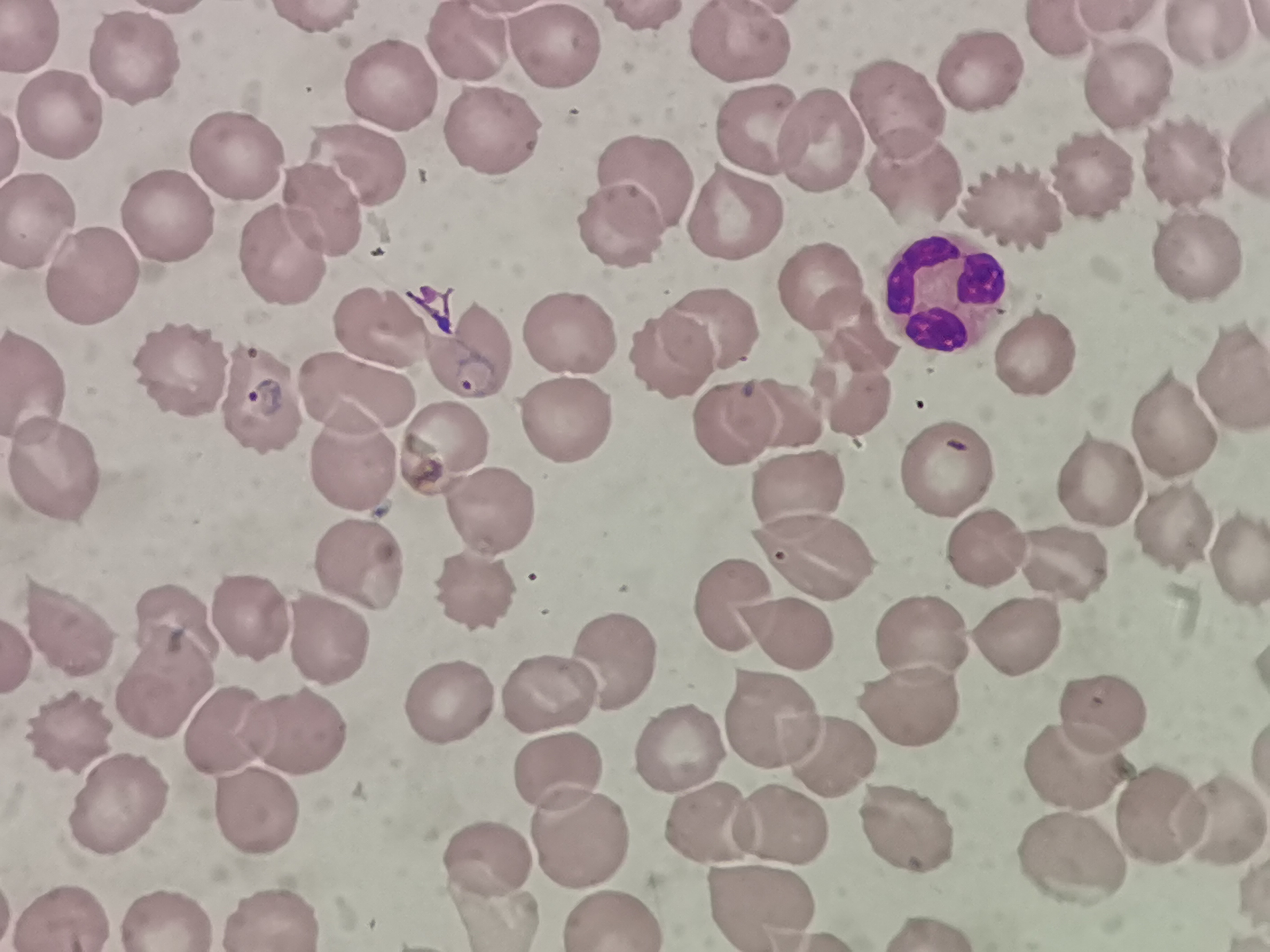
Approximate centers as {x, y} in pixels. Cell locations: {642, 18}, {321, 21}, {1058, 29}, {1203, 37}, {744, 44}, {467, 45}, {552, 47}, {136, 62}, {973, 72}, {1121, 85}, {391, 92}, {897, 109}, {63, 122}, {765, 134}, {817, 134}, {497, 138}, {236, 162}, {1180, 166}, {353, 171}, {1098, 175}, {911, 181}, {642, 186}, {1013, 197}, {324, 212}, {172, 216}, {738, 218}, {41, 223}, {618, 231}, {286, 257}, {1195, 258}, {86, 275}, {935, 287}, {823, 291}, {712, 324}, {855, 328}, {568, 329}, {387, 334}, {471, 350}, {1037, 352}, {671, 359}, {183, 372}, {1225, 378}, {36, 385}, {361, 390}, {852, 396}, {784, 412}, {562, 413}, {721, 426}, {1173, 431}, {437, 444}, {351, 456}, {946, 470}, {59, 474}, {798, 482}, {1092, 485}, {490, 511}, {1173, 525}, {812, 546}, {986, 554}, {1241, 557}, {1061, 562}, {356, 571}, {477, 593}, {731, 601}, {246, 621}, {70, 626}, {178, 630}, {786, 630}, {316, 637}, {1017, 638}, {921, 640}, {614, 654}, {158, 683}, {908, 695}, {550, 696}, {445, 700}, {1104, 707}, {768, 721}, {222, 729}, {295, 733}, {73, 736}, {675, 744}, {826, 753}, {1077, 760}, {556, 767}, {122, 799}, {251, 806}, {1157, 814}, {784, 817}, {1217, 817}, {911, 821}, {705, 822}, {577, 830}, {494, 854}, {1065, 855}, {756, 899}, {486, 903}, {275, 915}, {167, 916}, {616, 916}, {66, 917}. Giemsa stain. Thin smear of blood. Image is 1270×952 pixels. Single field of view. Photographed with a smartphone camera at the microscope eyepiece.